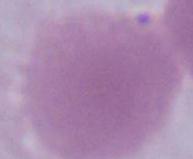
modality = photomicrograph
magnification = 1000x
identification = red blood cell